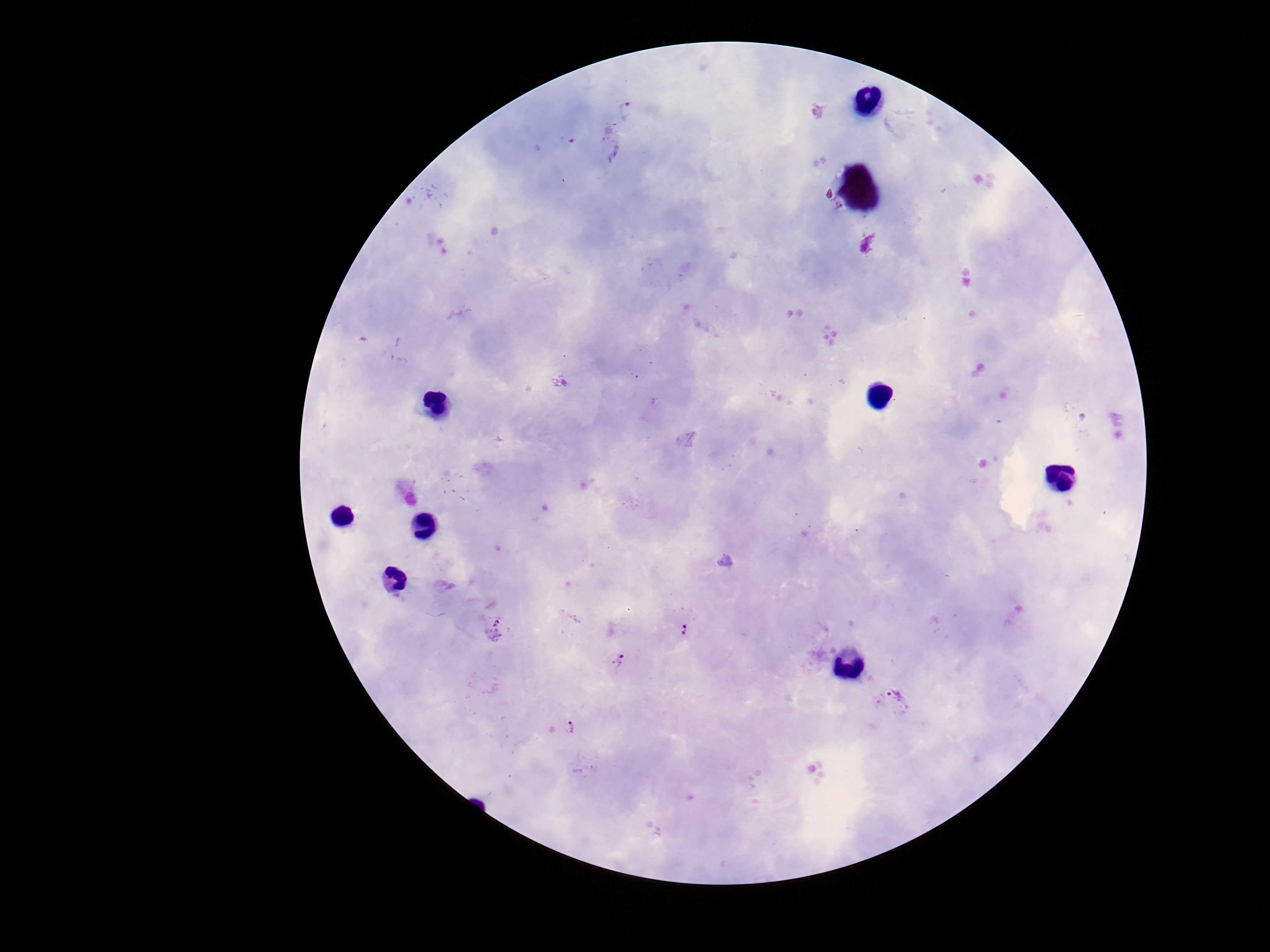

Approximate centers as [x, y] in pixels.
Summary:
  - Plasmodium parasite locations: [625, 110], [680, 626], [619, 659], [892, 702], [569, 727]
  - Stain: Giemsa
  - Capture: smartphone camera through the microscope eyepiece
  - Preparation: thick blood smear
  - Patient malaria status: positive
  - Image size: 1270×952 pixels
  - Field of view: one from this slide
  - Magnification: 100x